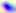

Summary:
  - Identification: Toxoplasma gondii
  - Magnification: 400x
  - Modality: photomicrograph